Describe the morphology of the red blood cells.
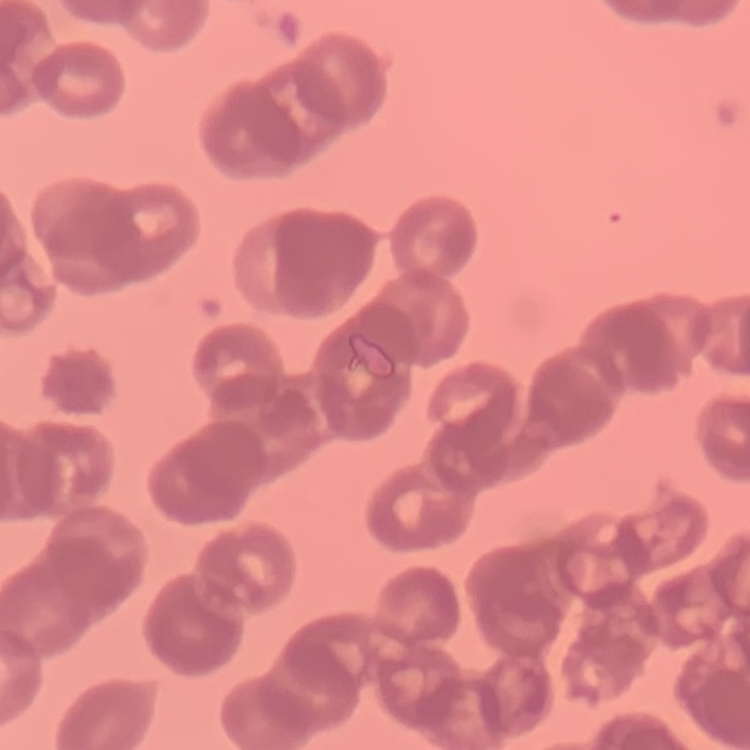
They show rouleaux formation.

image type = square crop of a larger photomicrograph
stain = Field's or Giemsa
preparation = thin blood smear